Report the malaria status of this cell.
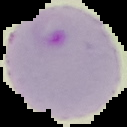
Parasitized.

Segmented cell region on a black background. Image is 127×127 pixels. From a thin blood film.